Classify this cell by malaria status.
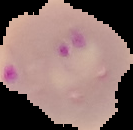

It is parasitized.

{
  "preparation": "thin blood film",
  "image_type": "segmented cell region with the area outside set to black",
  "image_size": "133×130 pixels"
}